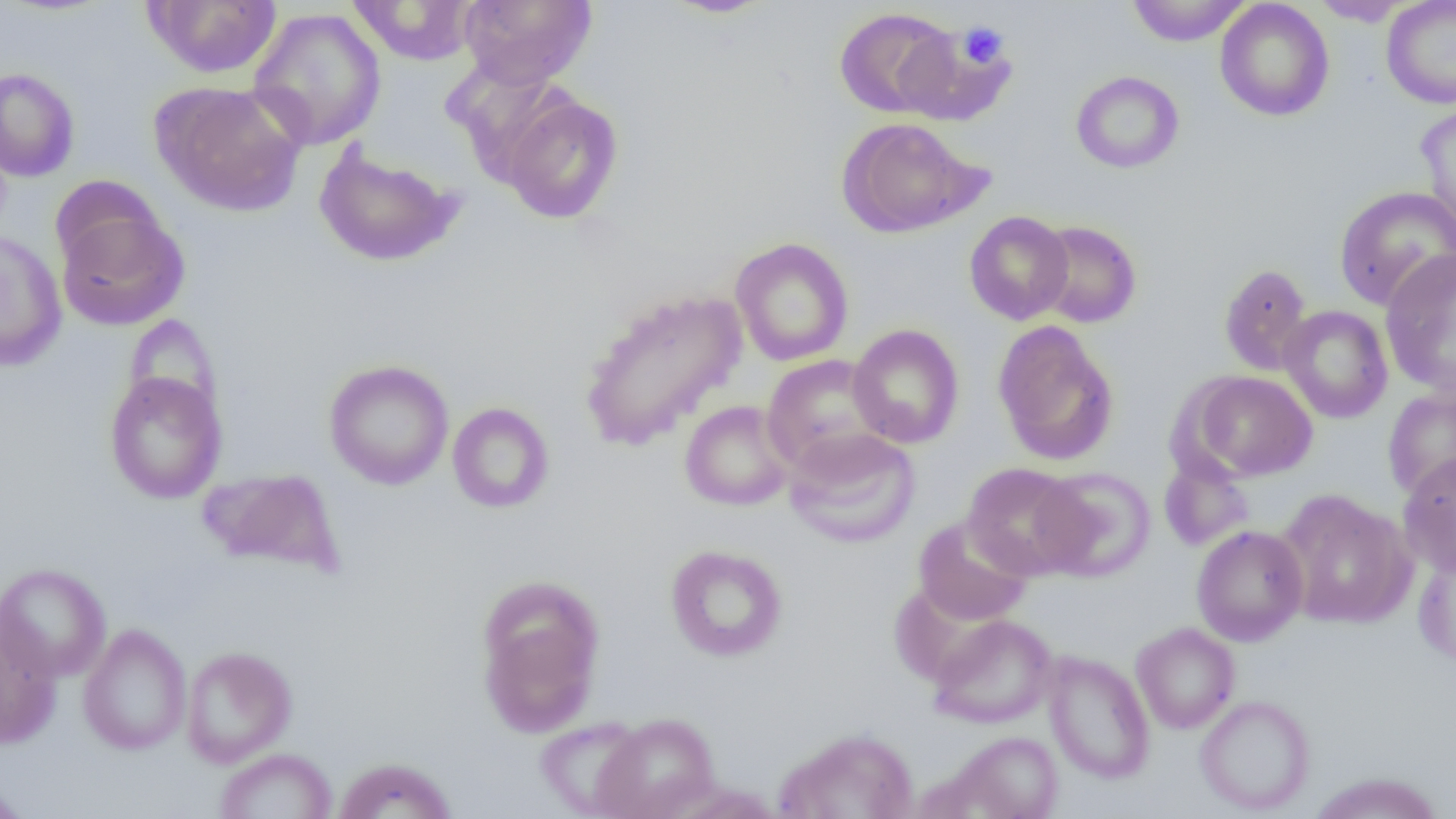
slide_level_diagnosis: no evidence of blood parasites
uninfected_red_blood_cell_locations: 'approximate bounding boxes as (x1,y1)-(x2,y2) corner pairs in pixels: (143,0)-(283,78), (458,0)-(597,89), (661,0)-(774,18), (1126,0)-(1251,46), (1215,0)-(1334,122), (1381,0)-(1456,109), (347,1)-(479,65), (1312,1)-(1412,26), (248,7)-(386,150), (834,7)-(960,118), (0,68)-(80,181), (1070,70)-(1184,173), (151,81)-(306,217), (498,91)-(624,224), (1415,102)-(1456,238), (836,117)-(984,239), (313,141)-(464,268), (1334,185)-(1456,311), (55,201)-(189,332), (964,211)-(1074,325), (1031,220)-(1142,328), (0,231)-(67,371), (730,237)-(854,366), (1379,249)-(1456,398), (1219,263)-(1313,376), (577,286)-(748,452), (1279,305)-(1393,424), (124,314)-(223,420), (992,321)-(1119,465), (848,324)-(965,449), (761,354)-(890,474), (323,359)-(455,490), (104,371)-(228,504), (1189,371)-(1317,482), (1382,387)-(1456,501), (679,400)-(795,511), (447,402)-(554,513), (783,427)-(921,549), (1398,452)-(1456,577), (1158,454)-(1254,551), (962,462)-(1088,579), (1034,467)-(1157,582), (198,468)-(347,576), (1276,490)-(1416,629), (912,515)-(1034,626), (1191,525)-(1309,646), (665,544)-(788,661), (1413,547)-(1456,668), (0,562)-(111,683), (476,586)-(603,737), (0,613)-(61,748), (927,614)-(1058,729), (1131,623)-(1240,734), (77,624)-(192,756), (181,646)-(297,767), (1043,651)-(1155,784), (1195,695)-(1315,815), (593,712)-(720,819), (534,717)-(649,818), (776,728)-(919,819), (947,731)-(1063,818), (215,748)-(338,819), (332,757)-(457,819), (1308,772)-(1446,818), (0,778)-(31,818)'
modality: optical microscopy
magnification: 1000x
platelet_locations: 'approximate bounding boxes as (x1,y1)-(x2,y2) corner pairs in pixels: (956,21)-(1008,70)'
preparation: thin blood film
image_size: 1456×819 pixels
field_of_view: one of a larger specimen